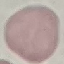
Result: no malaria parasites seen. Giemsa-stained preparation. Acquired by smartphone through the microscope eyepiece. Thin smear of blood. Automatically extracted cell patch, resized to 64 × 64 pixels.